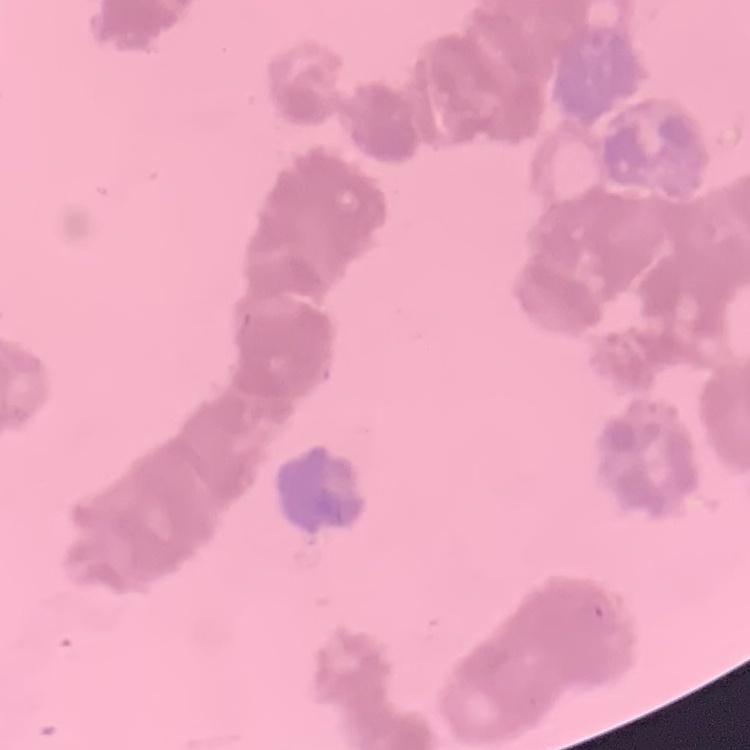

The red blood cells exhibit rouleaux formation. Thin blood smear. Square crop of a larger photomicrograph. Field's or Giemsa stain.